Assess this cell for malaria.
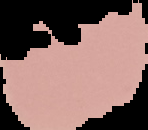
It is uninfected.

Image is 148×130 pixels. From a thin blood film. Segmented cell region on a black background.